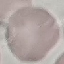

Summary:
  - Malaria status: uninfected
  - Image type: cell patch, automatically extracted from a larger field of view and resized to 64 × 64 pixels
  - Capture: smartphone through the microscope eyepiece
  - Stain: Giemsa
  - Preparation: thin smear